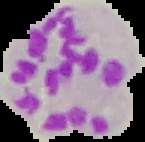

Summary:
  - Result: malaria parasites detected
  - Image size: 145×142 pixels
  - Image type: cell region segmented out of the field of view; surrounding area masked to black
  - Preparation: thin blood smear